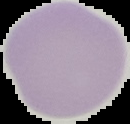
Summary:
  - Result: no malaria parasites seen
  - Image size: 130×124 pixels
  - Image type: cell region segmented out of the field of view; surrounding area masked to black
  - Preparation: thin blood film